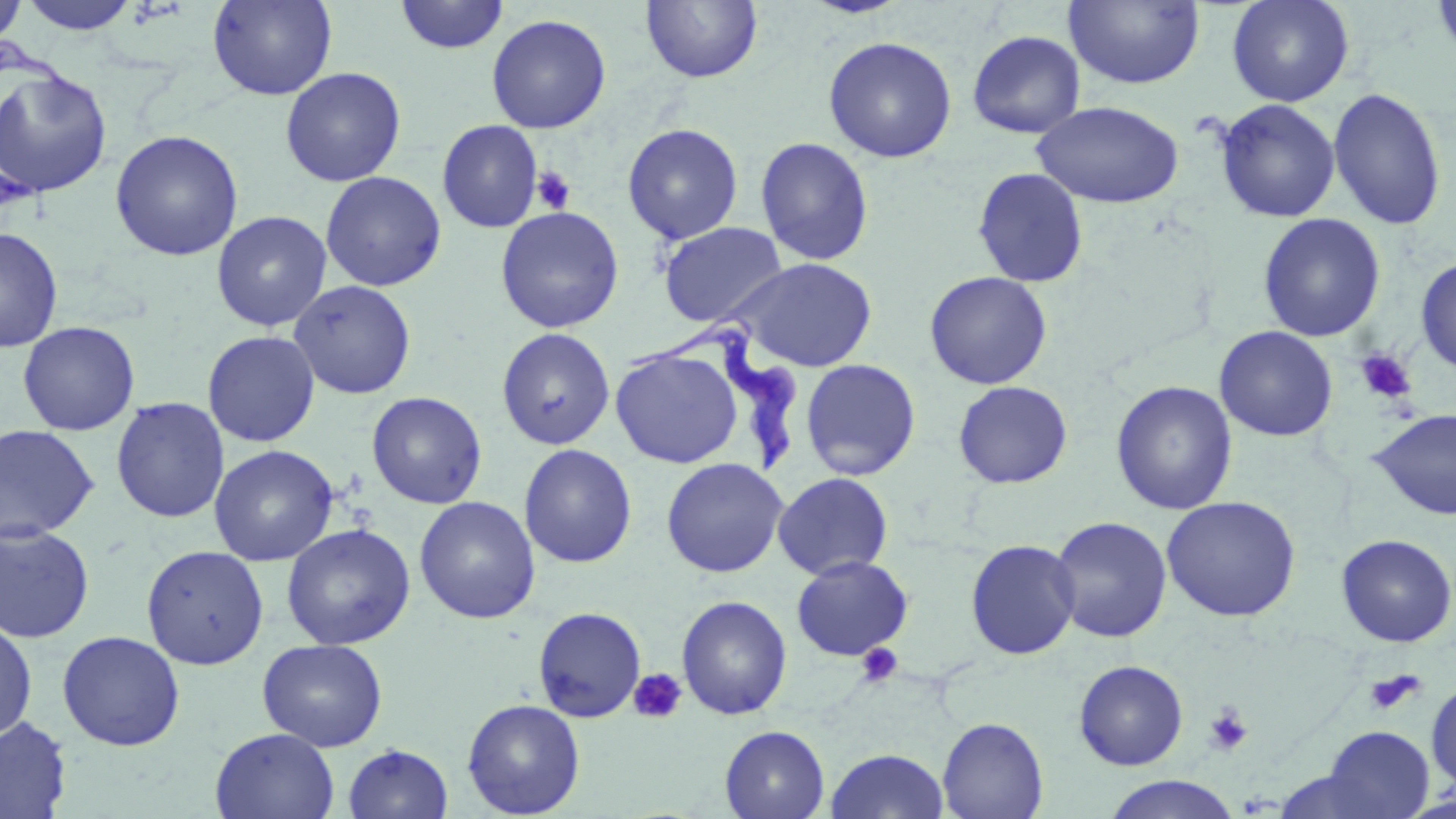
Summary:
  - Coordinate format: approximate bounding boxes as (x1, y1, x2, y2) in pixels
  - Platelet locations: (530, 166, 576, 215), (1354, 348, 1417, 405), (855, 642, 904, 689), (628, 668, 687, 724), (1363, 669, 1424, 716), (1203, 704, 1253, 756)
  - Uninfected red blood cell locations: (0, 0, 27, 48), (17, 0, 141, 35), (207, 0, 337, 100), (394, 0, 509, 54), (641, 0, 763, 84), (802, 0, 912, 19), (1064, 0, 1205, 90), (1226, 0, 1354, 107), (1430, 0, 1456, 67), (486, 14, 611, 134), (967, 30, 1086, 139), (823, 36, 957, 163), (280, 67, 406, 187), (0, 69, 113, 198), (1328, 85, 1447, 232), (1215, 99, 1341, 223), (1032, 100, 1184, 208), (437, 120, 543, 233), (622, 123, 743, 245), (109, 129, 244, 261), (754, 137, 875, 267), (972, 167, 1089, 288), (320, 171, 446, 292), (495, 206, 624, 333), (211, 210, 332, 331), (1258, 213, 1385, 342), (658, 222, 788, 328), (0, 228, 63, 352), (1415, 255, 1456, 376), (728, 258, 877, 372), (924, 271, 1053, 390), (288, 280, 417, 399), (17, 321, 140, 435), (1214, 326, 1338, 442), (496, 328, 615, 450), (202, 330, 320, 447), (610, 347, 742, 469), (800, 358, 921, 481), (953, 380, 1073, 489), (1111, 380, 1238, 515), (366, 391, 487, 509), (110, 397, 229, 523), (1367, 408, 1456, 520), (0, 424, 100, 544), (519, 443, 637, 568), (209, 445, 338, 566), (661, 458, 788, 577), (773, 472, 894, 580), (414, 496, 541, 624), (1162, 496, 1301, 622), (1048, 515, 1172, 643), (0, 522, 95, 643), (280, 523, 416, 650), (1336, 534, 1456, 648), (965, 538, 1081, 660), (141, 545, 269, 670), (791, 556, 913, 660), (676, 595, 793, 720), (532, 606, 646, 723), (0, 617, 37, 741), (56, 630, 185, 751), (257, 638, 388, 751), (1073, 660, 1189, 771), (1426, 680, 1456, 792), (462, 698, 585, 818), (0, 716, 72, 818), (937, 716, 1049, 819), (720, 725, 830, 819), (1319, 725, 1434, 818), (210, 727, 340, 819), (343, 744, 453, 819), (825, 747, 950, 819), (1104, 775, 1239, 818)
  - Trypanosoma brucei locations: (624, 317, 809, 476)
  - Slide-level diagnosis: Trypanosoma brucei
  - Preparation: thin blood smear
  - Magnification: 1000x
  - Field of view: single
  - Stain: May-Grünwald-Giemsa
  - Image size: 1456×819 pixels
  - Modality: optical microscopy